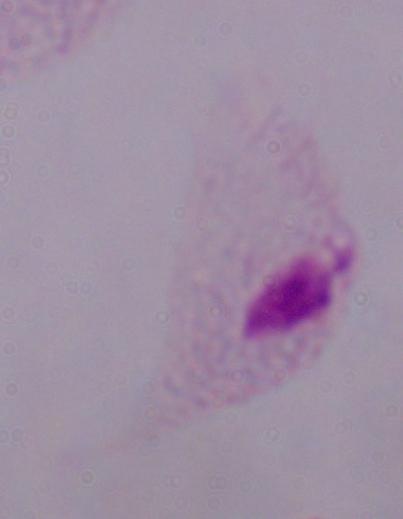

modality: photomicrograph
magnification: 1000x
identification: trichomonad